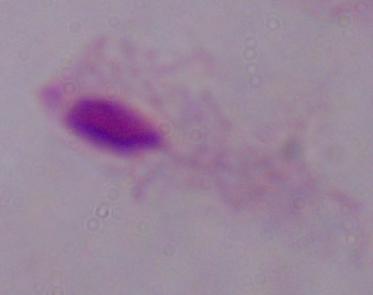
Summary:
  - Magnification: 1000x
  - Identification: trichomonad
  - Modality: micrograph